Give the position of every Plasmodium parasite visible.
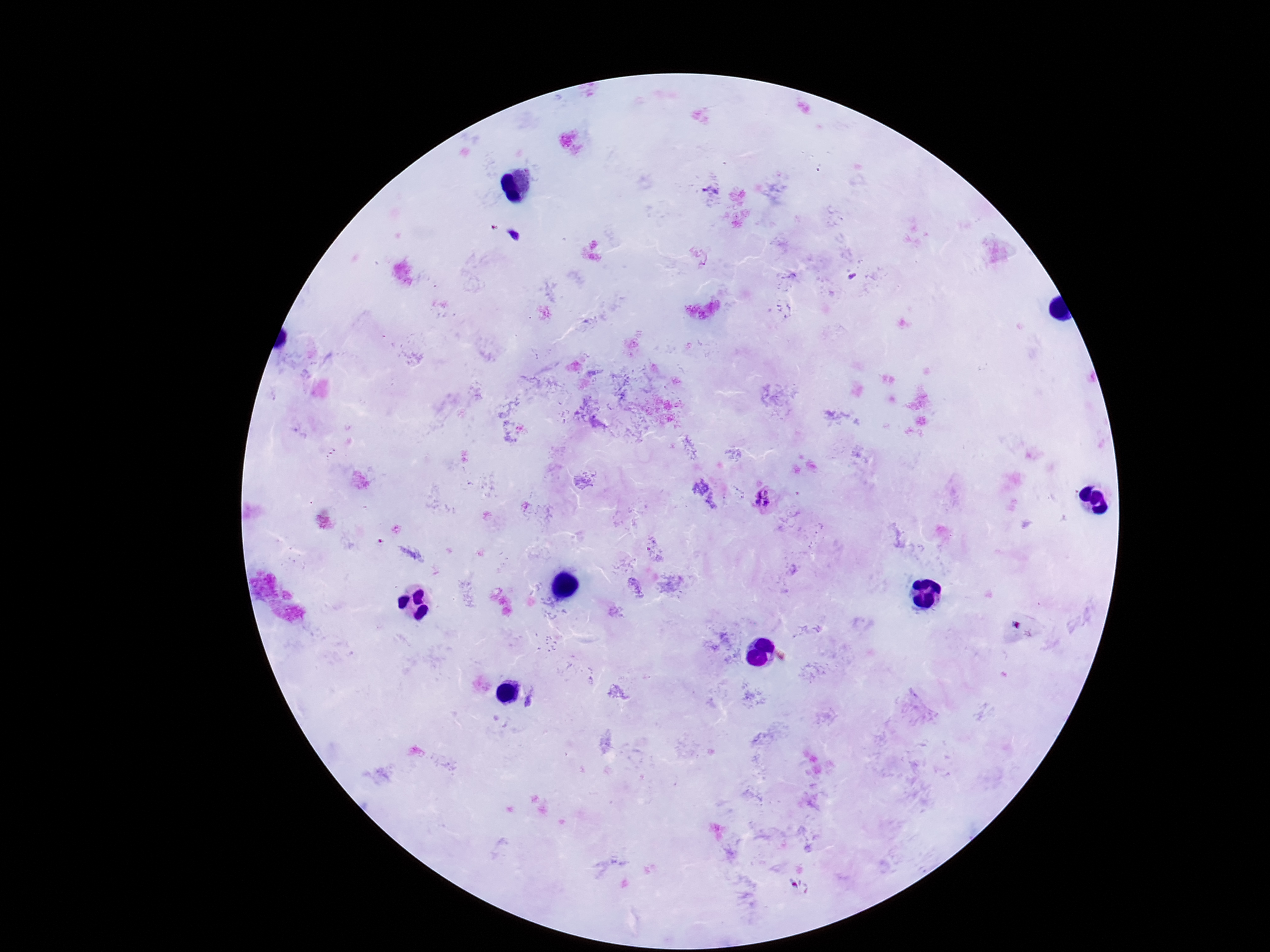
Approximate centers as {x, y} in pixels.
Plasmodium parasites: {711, 191}, {765, 501}.

preparation = thick blood smear
field of view = one from this slide
magnification = 100x
image size = 1270×952 pixels
capture = smartphone camera through the microscope eyepiece
patient malaria status = positive
stain = Giemsa